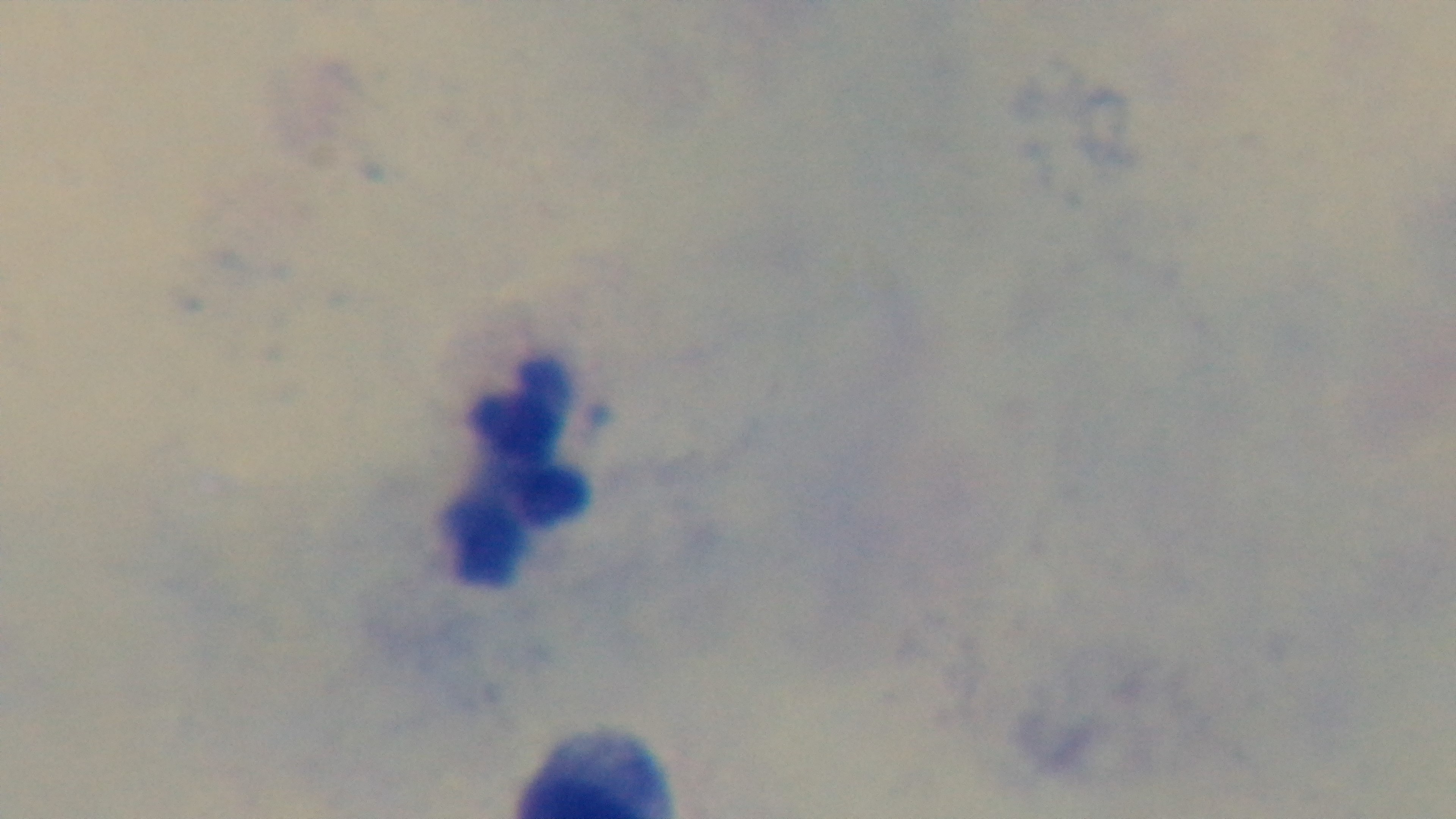

Summary:
  - Malaria status: negative
  - Field of view: single
  - Capture: mounted 4K digital camera
  - Preparation: thick blood film
  - Stain: Giemsa
  - Objective: 100x oil immersion
  - Modality: light microscopy